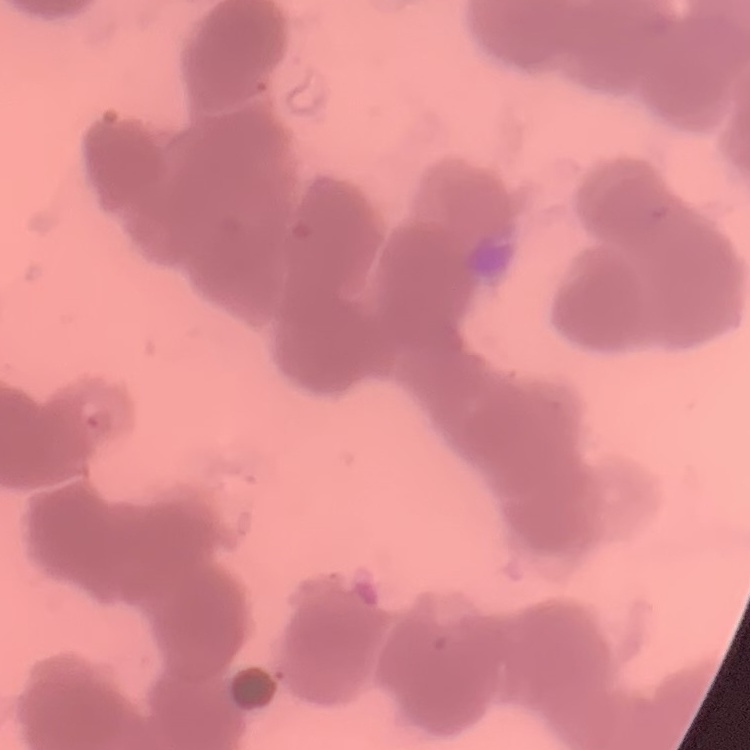

The red blood cells show rouleaux formation. Thin blood film. Field's or Giemsa stain. Square crop of a larger photomicrograph.